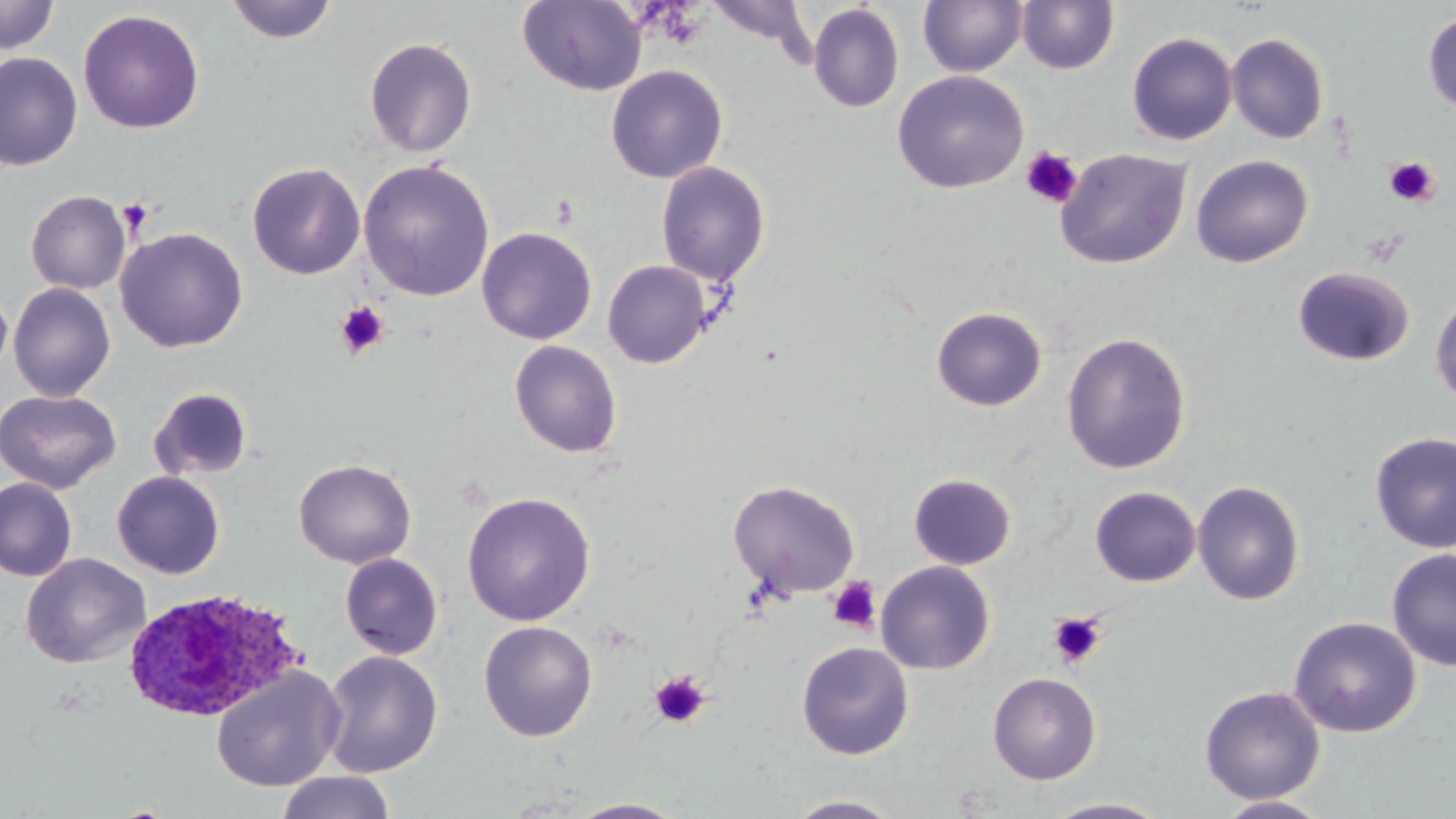 Approximate bounding boxes as [x1, y1, x2, y2] in pixels. Platelet locations: [1020, 147, 1083, 208], [1384, 156, 1440, 208], [116, 198, 152, 233], [336, 302, 389, 358], [827, 576, 882, 634], [1047, 611, 1108, 669], [649, 671, 711, 729]. Plasmodium ovale-infected red blood cell locations: [121, 588, 301, 724]. Uninfected red blood cell locations: [0, 0, 60, 55], [225, 0, 338, 44], [703, 0, 817, 57], [917, 0, 1029, 77], [517, 1, 647, 96], [1016, 1, 1119, 74], [808, 3, 905, 113], [78, 9, 204, 134], [1422, 9, 1456, 114], [1126, 32, 1237, 145], [1226, 33, 1330, 144], [363, 36, 478, 157], [0, 52, 83, 171], [606, 64, 728, 184], [892, 70, 1029, 194], [1055, 147, 1191, 270], [1191, 154, 1313, 268], [358, 158, 495, 302], [656, 161, 772, 286], [247, 162, 365, 279], [26, 190, 131, 294], [476, 226, 598, 345], [114, 227, 249, 353], [602, 260, 712, 368], [1291, 266, 1415, 368], [7, 282, 116, 401], [0, 283, 12, 381], [1429, 289, 1456, 407], [931, 306, 1048, 412], [1060, 332, 1193, 474], [509, 339, 623, 458], [148, 386, 255, 481], [0, 389, 121, 494], [1369, 431, 1456, 553], [294, 458, 416, 568], [112, 471, 225, 579], [908, 473, 1016, 570], [0, 477, 77, 583], [727, 479, 861, 599], [1192, 479, 1305, 606], [1089, 486, 1201, 587], [462, 492, 596, 626], [1386, 548, 1456, 671], [20, 553, 150, 669], [339, 553, 444, 660], [875, 561, 996, 674], [1288, 616, 1421, 737], [478, 621, 597, 742], [796, 641, 914, 760], [320, 650, 443, 778], [211, 666, 345, 792], [987, 672, 1101, 785], [1199, 686, 1325, 805], [275, 771, 397, 819], [781, 794, 909, 818], [1212, 795, 1333, 818], [1037, 797, 1173, 818], [564, 798, 688, 818]. Slide-level diagnosis: Plasmodium ovale. Light microscopy. Single field of view. May-Grünwald-Giemsa stain. Image is 1456×819 pixels. Thin blood smear. 1000x magnification.